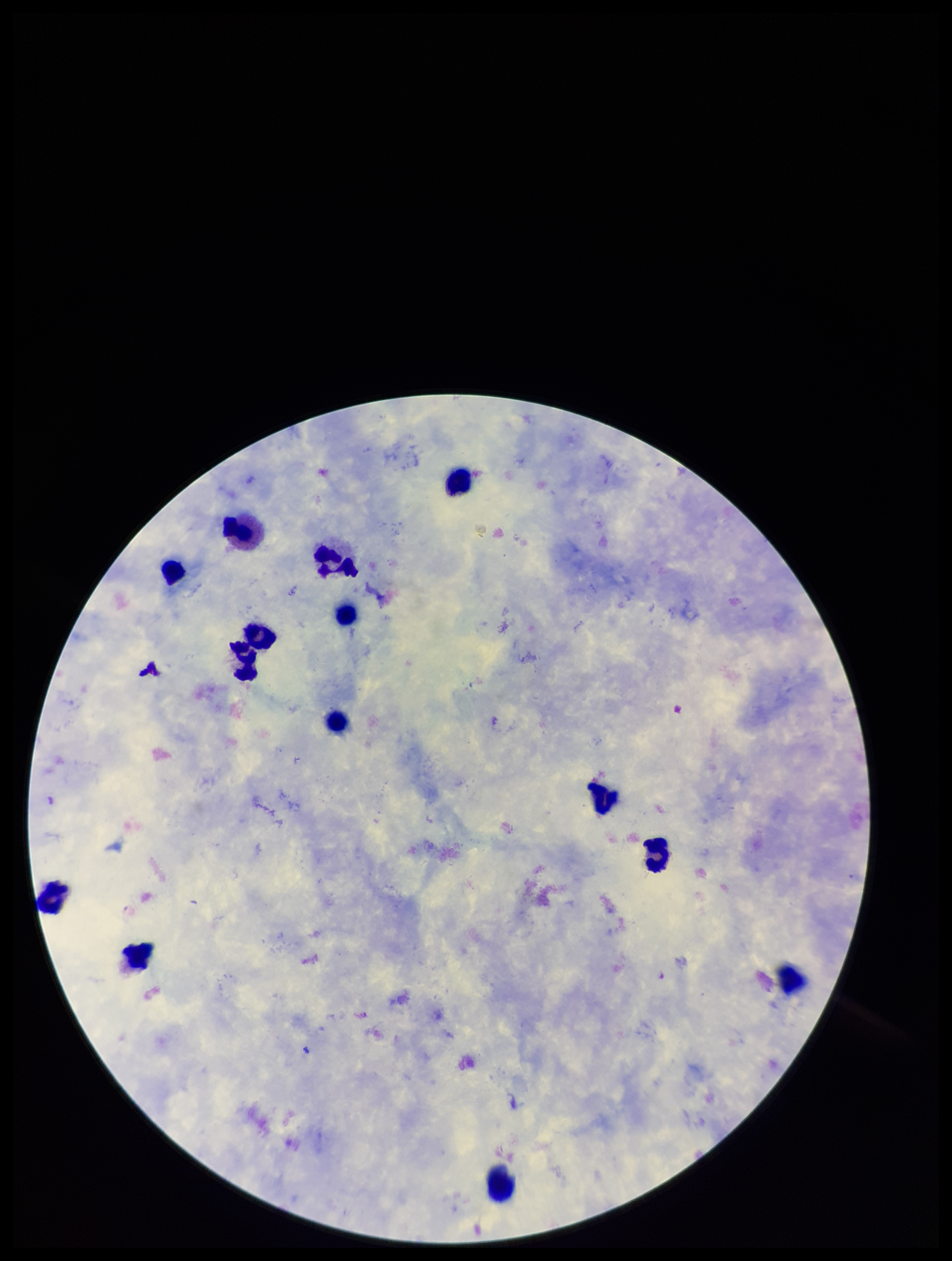
Summary:
  - Field of view: one from this slide
  - Preparation: thick blood smear
  - Image size: 952×1261 pixels
  - Parasite count: 0
  - Patient malaria status: infected
  - Species reported for this patient: Plasmodium falciparum
  - Capture: smartphone photograph through the microscope eyepiece
  - Stain: Giemsa
  - Plasmodium parasites: none detected
  - Leukocyte count: 14